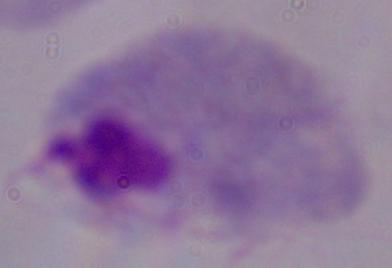
1000x magnification. A trichomonad is seen. Micrograph.